Outline each P. falciparum parasite and classify it by life-cycle stage.
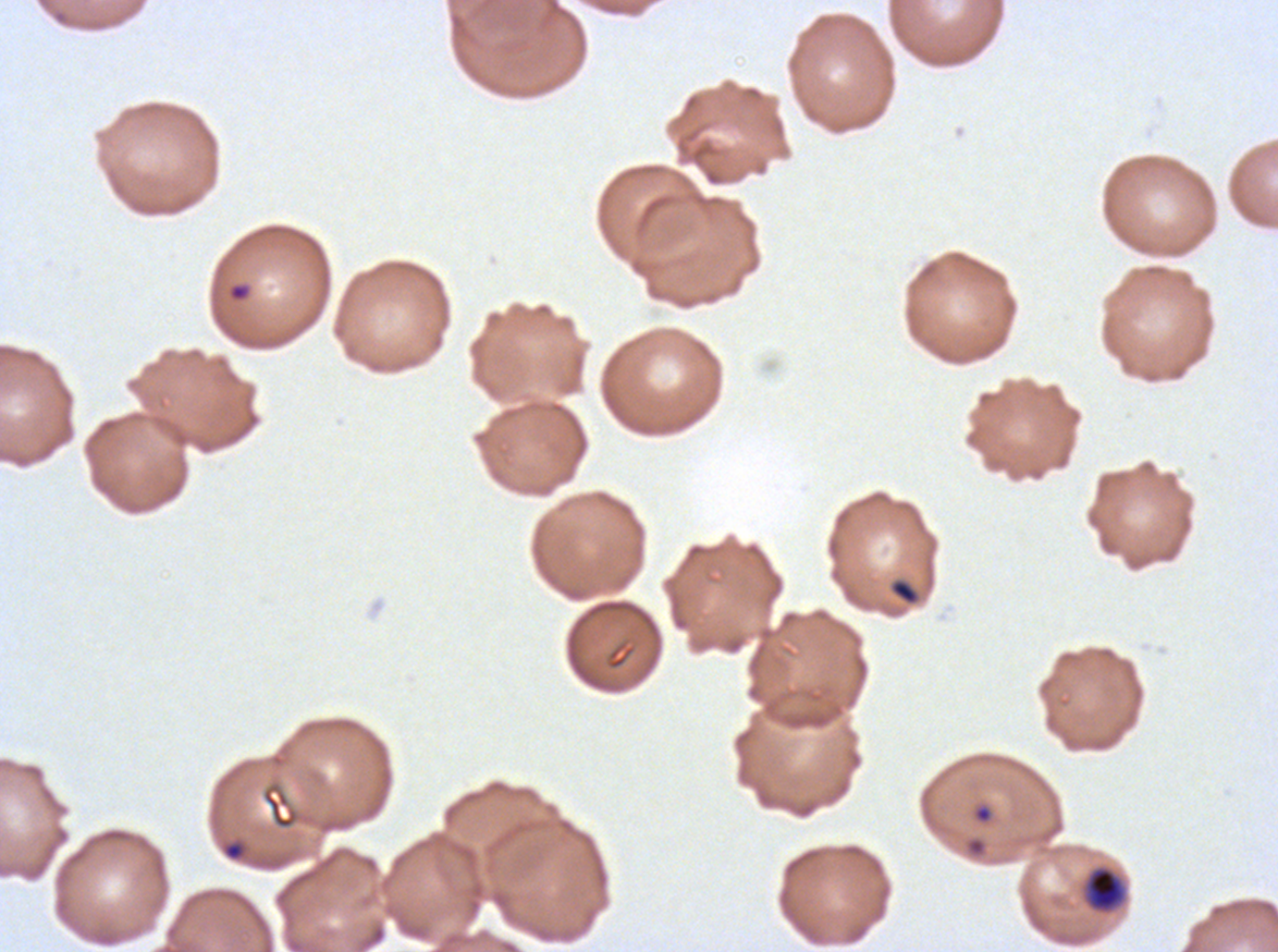
Approximate bounding boxes as {x1, y1, x2, y2} in pixels.
Rings: {227, 282, 252, 302}, {261, 782, 300, 830}, {973, 804, 993, 824}.
Late-ring/early-trophozoite forms: {1086, 867, 1124, 911}.
No mid trophozoites, late trophozoites, early schizonts, late schizonts, segmenters, or gametocytes observed.

Summary:
  - Debris locations: {889, 578, 920, 605}
  - Preparation: thin blood film
  - Specimen: P. falciparum cultured ex vivo for 24 to 48 hours, from a patient in The Gambia
  - Image size: 1278×952 pixels
  - Field of view: sub-image separated from a larger composite
  - Life-cycle stages observed: ring, late-ring/early-trophozoite
  - Stain: Giemsa